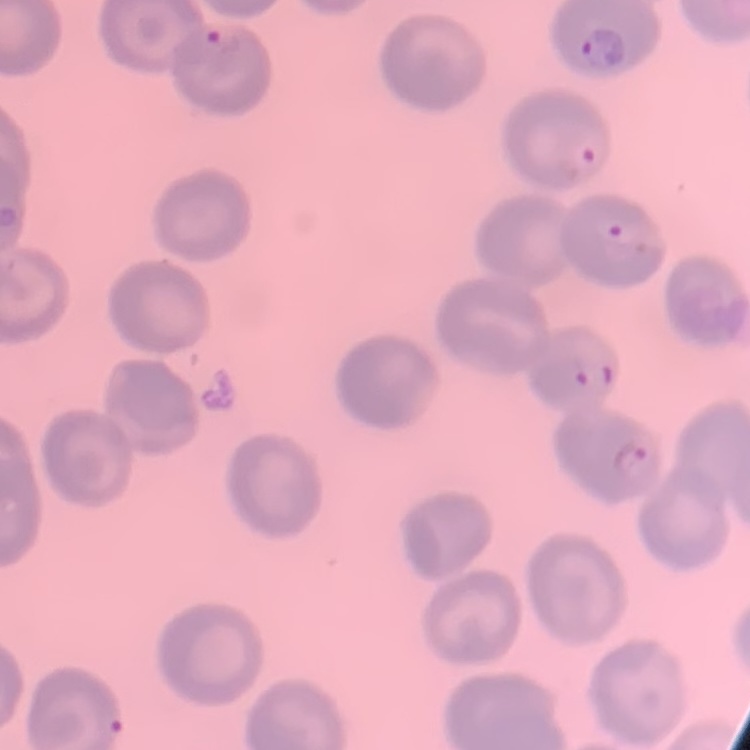
The erythrocytes show no rouleaux formation. Stained with either Field's or Giemsa. Thin blood smear. One tile cut from a larger photomicrograph.